Classify this cell by malaria status.
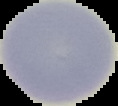
It is uninfected.

image_type: segmented cell region with the area outside set to black
preparation: thin blood film
image_size: 118×106 pixels